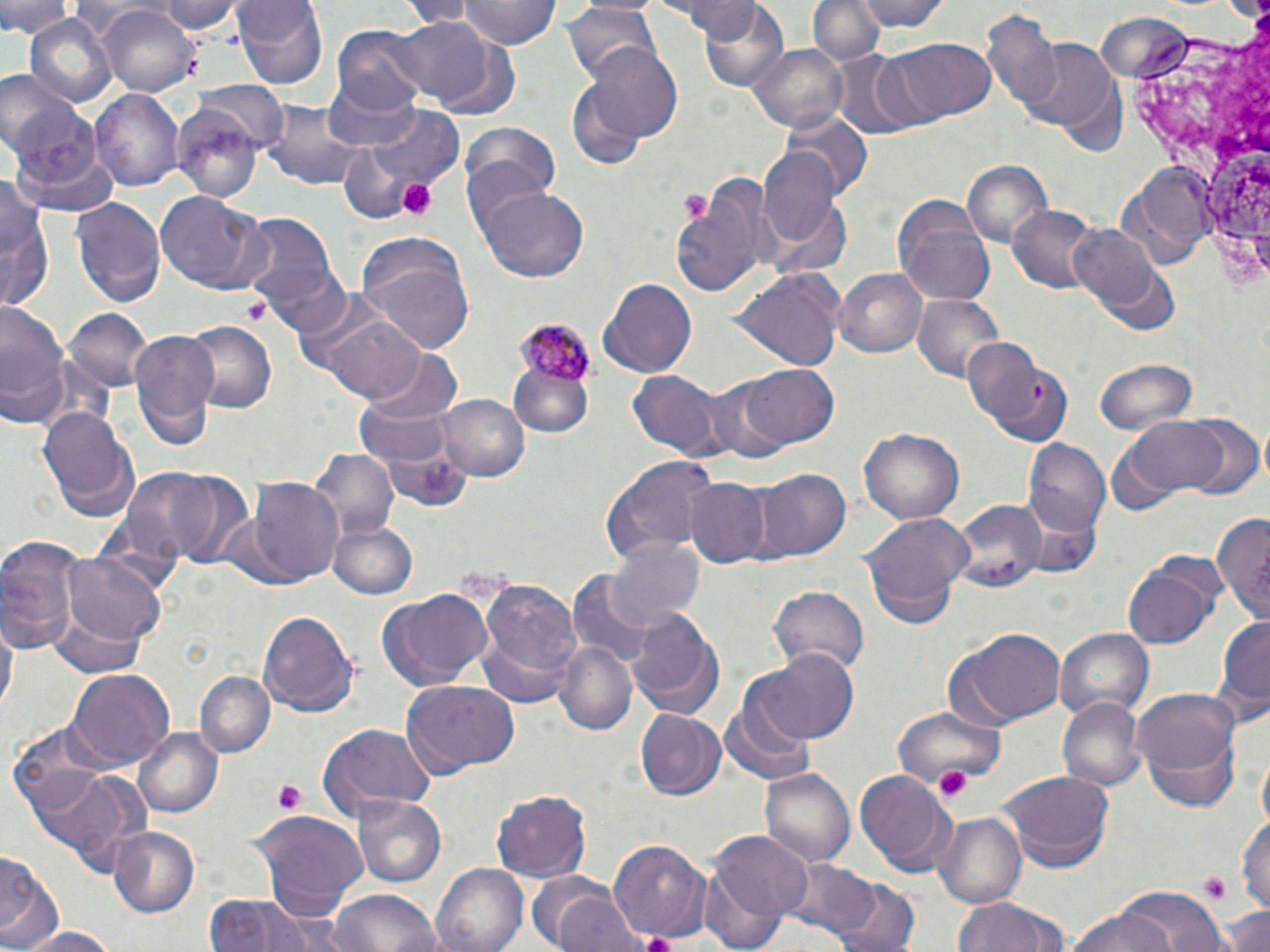 Approximate bounding boxes as (x1,y1)-(x2,y2) corner pairs in pixels. Uninfected red blood cell locations: (0,0)-(71,40), (155,0)-(243,36), (231,0)-(328,91), (388,0)-(483,24), (459,0)-(557,49), (668,0)-(766,40), (807,0)-(886,67), (849,0)-(952,30), (815,1)-(932,50), (561,4)-(661,83), (698,4)-(789,95), (100,6)-(199,97), (981,8)-(1066,115), (25,13)-(117,106), (389,19)-(493,102), (333,24)-(433,117), (893,36)-(996,121), (432,39)-(520,118), (1022,39)-(1120,136), (748,42)-(851,133), (580,44)-(686,145), (830,52)-(927,139), (568,69)-(658,165), (323,77)-(422,150), (195,83)-(287,155), (90,89)-(184,194), (6,102)-(108,201), (261,102)-(367,191), (359,106)-(465,201), (171,107)-(262,200), (783,109)-(870,199), (462,124)-(562,215), (333,142)-(427,222), (758,149)-(843,250), (962,161)-(1053,249), (1124,165)-(1216,262), (673,171)-(776,297), (0,174)-(51,309), (477,185)-(590,286), (156,190)-(272,294), (71,197)-(165,307), (894,198)-(995,303), (1009,206)-(1103,293), (236,210)-(342,313), (1070,224)-(1167,317), (354,237)-(475,353), (249,254)-(352,339), (730,267)-(846,369), (834,267)-(926,358), (601,278)-(696,378), (911,294)-(1008,383), (0,300)-(69,428), (63,308)-(150,391), (320,309)-(428,403), (182,320)-(275,413), (127,329)-(220,448), (963,337)-(1069,446), (360,344)-(465,457), (1091,359)-(1198,435), (513,361)-(590,434), (737,362)-(838,448), (628,372)-(725,459), (701,375)-(792,464), (438,393)-(529,482), (36,403)-(139,522), (1174,415)-(1265,499), (1112,417)-(1235,509), (860,425)-(965,524), (1025,440)-(1112,538), (309,447)-(398,543), (599,455)-(719,564), (140,467)-(256,567), (754,468)-(850,563), (248,480)-(343,586), (686,480)-(772,565), (950,500)-(1049,591), (1212,509)-(1270,615), (862,512)-(971,627), (327,519)-(419,600), (0,536)-(85,653), (609,537)-(705,633), (63,552)-(168,647), (1120,557)-(1221,651), (565,572)-(655,671), (475,577)-(581,696), (768,586)-(869,675), (376,591)-(495,690), (625,607)-(726,719), (49,610)-(150,677), (257,610)-(358,714), (1210,613)-(1270,728), (2,615)-(17,718), (955,628)-(1067,726), (1056,628)-(1152,722), (554,642)-(637,738), (758,649)-(862,744), (67,668)-(173,768), (195,671)-(273,756), (400,682)-(521,777), (1133,688)-(1240,812), (719,693)-(818,785), (1057,693)-(1146,791), (635,707)-(725,800), (892,708)-(1002,784), (10,721)-(109,818), (317,722)-(435,819), (135,727)-(223,817), (32,767)-(143,868), (760,768)-(854,866), (1000,769)-(1114,870), (854,772)-(953,870), (492,788)-(594,881), (355,797)-(446,887), (1238,806)-(1270,918), (933,811)-(1027,908), (253,812)-(369,919), (109,827)-(201,917), (708,831)-(812,930), (609,837)-(711,940), (0,850)-(60,950), (782,859)-(882,943), (431,863)-(527,952), (698,864)-(790,952), (832,879)-(919,952), (544,886)-(646,952), (1111,886)-(1229,952), (327,889)-(446,952), (205,892)-(321,952), (951,894)-(1069,952), (1218,903)-(1270,952), (1066,905)-(1182,952), (10,923)-(122,952). Plasmodium malariae-infected red blood cell locations: (516,319)-(590,399). Platelet locations: (394,175)-(438,219), (678,186)-(714,226), (241,296)-(270,327), (935,764)-(974,803), (271,778)-(310,815), (1199,875)-(1232,905). Slide-level diagnosis: Plasmodium malariae. Image is 1270×952 pixels. Single field of view. Light microscopy. May-Grünwald-Giemsa-stained preparation. 1000x magnification. Thin blood smear.